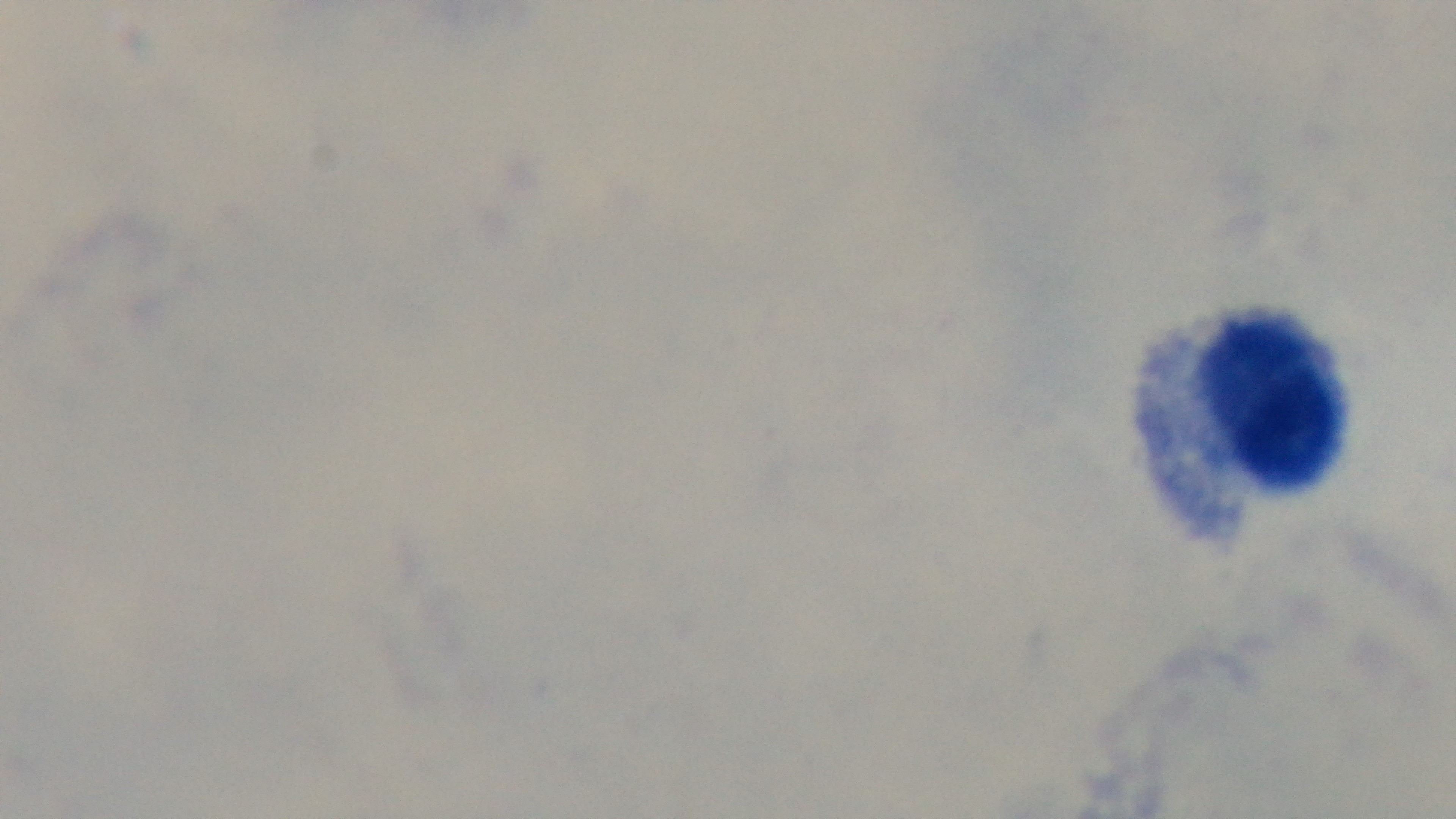 One field from the slide. Malaria status: negative. Preparation: thick. Giemsa-stained. 100x oil-immersion objective. Light microscopy. Mounted 4K digital camera.